Assess this cell for malaria.
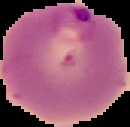
Parasitized.

image size = 130×127 pixels
image type = segmented cell region on a black background
preparation = thin blood smear